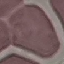
{
  "result": "no malaria parasites detected",
  "image_type": "cell patch, automatically extracted from a larger field of view and resized to 64 × 64 pixels",
  "capture": "smartphone through the microscope eyepiece",
  "stain": "Giemsa",
  "preparation": "thin blood smear"
}